Locate every Plasmodium parasite.
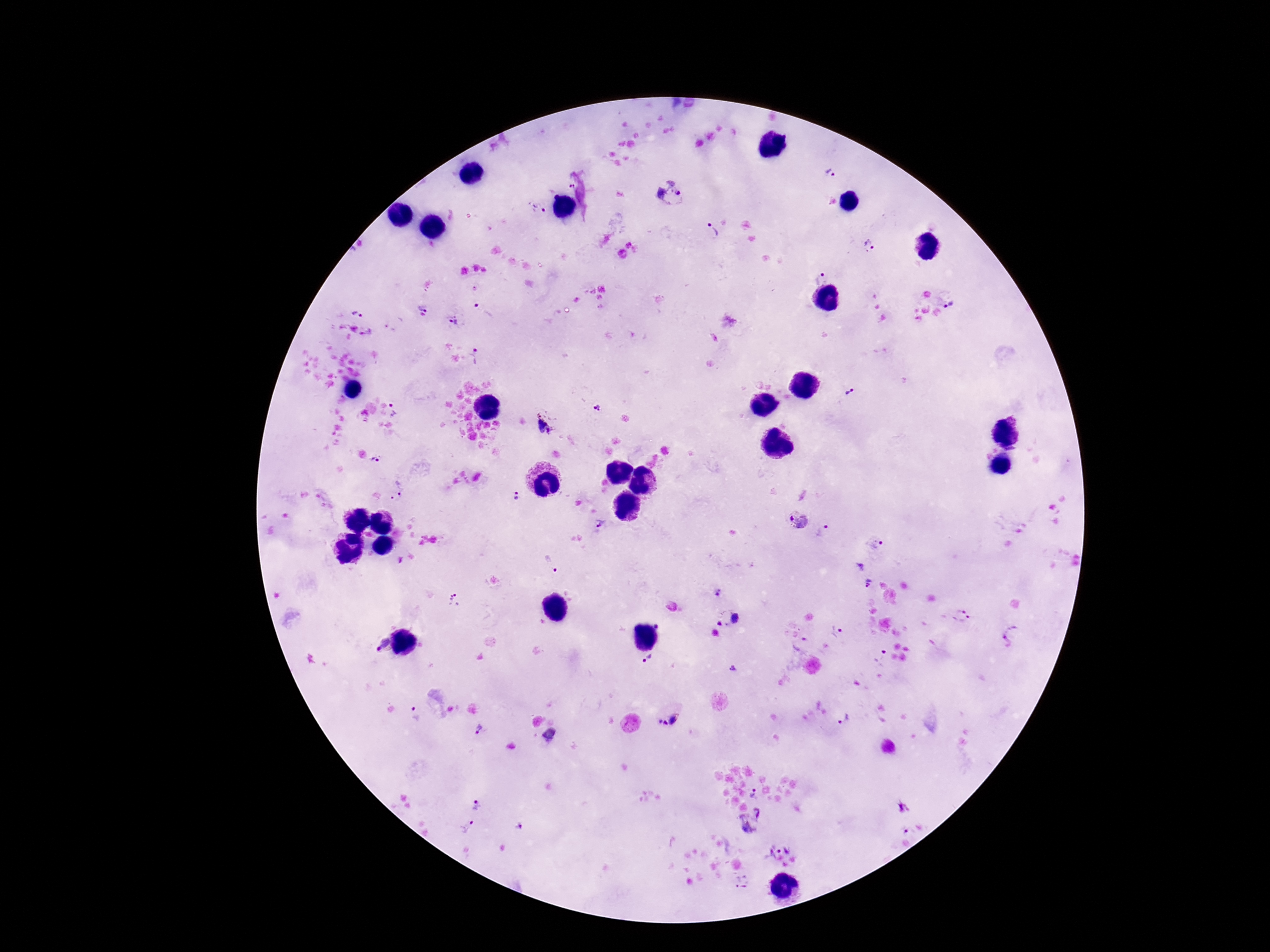

Approximate centers as {x, y} in pixels.
Plasmodium parasites: {829, 174}, {569, 186}, {669, 192}, {536, 209}, {710, 231}, {869, 245}, {815, 276}, {949, 303}, {424, 304}, {484, 311}, {359, 314}, {453, 320}, {478, 355}, {850, 391}, {598, 407}, {395, 409}, {544, 424}, {374, 460}, {400, 486}, {518, 495}, {796, 519}, {600, 523}, {824, 531}, {876, 543}, {556, 571}, {869, 583}, {719, 592}, {456, 600}, {961, 616}, {736, 618}, {722, 622}, {658, 626}, {837, 634}, {1012, 638}, {383, 644}, {801, 645}, {879, 657}, {648, 659}, {733, 669}, {414, 714}, {674, 718}, {844, 718}, {660, 722}, {665, 723}, {478, 729}, {752, 794}, {476, 806}, {752, 819}, {519, 826}, {468, 828}, {779, 849}, {742, 882}.

Single field of view. 100x magnification. Thick peripheral-blood smear. Smartphone photograph taken through the microscope eyepiece. Giemsa-stained preparation. Image is 1270×952 pixels. Patient malaria status: positive.